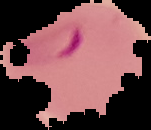
The area outside the segmented cell region is set to black. Image is 151×130 pixels. From a thin blood film. Result: Plasmodium parasites detected.